Locate every blood parasite and identify its species.
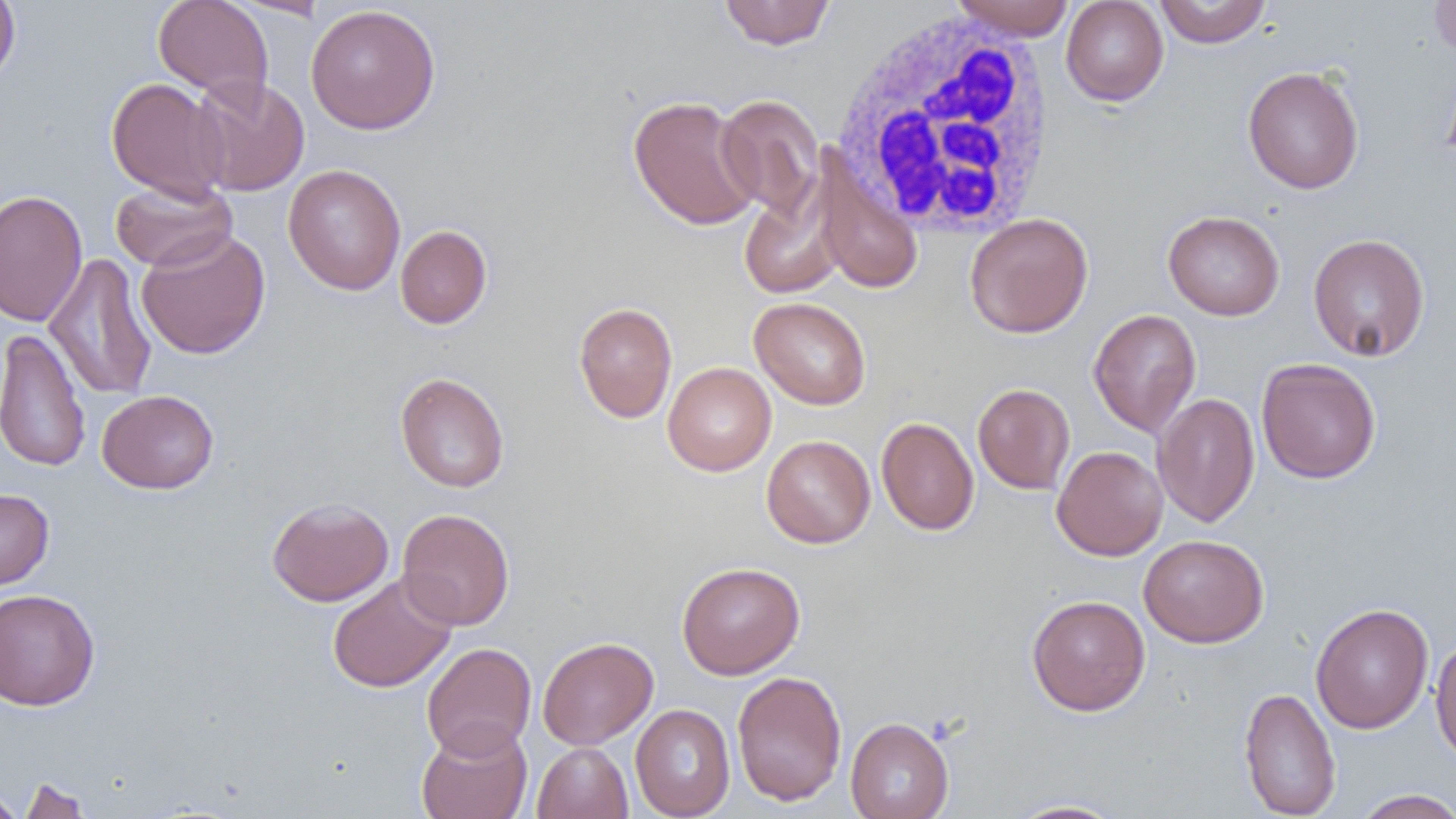
No blood parasites observed.

Summary:
  - Coordinate format: approximate bounding boxes as [x1, y1, x2, y2] in pixels
  - White blood cell locations: [828, 11, 1061, 242]
  - Uninfected red blood cell locations: [0, 0, 20, 87], [718, 0, 836, 50], [951, 0, 1076, 40], [1153, 0, 1272, 47], [1429, 0, 1456, 58], [153, 1, 273, 99], [1061, 1, 1169, 106], [305, 4, 441, 135], [1442, 62, 1456, 176], [1242, 66, 1364, 194], [189, 75, 310, 197], [106, 77, 230, 201], [716, 94, 825, 222], [628, 95, 761, 231], [812, 152, 924, 295], [283, 164, 406, 295], [109, 178, 237, 272], [739, 181, 847, 299], [0, 190, 87, 327], [1163, 210, 1285, 320], [964, 213, 1094, 338], [394, 225, 493, 328], [136, 228, 271, 360], [1307, 233, 1430, 362], [43, 253, 158, 400], [749, 297, 871, 409], [573, 302, 677, 423], [1088, 308, 1202, 437], [0, 328, 91, 473], [1256, 357, 1381, 484], [662, 362, 776, 476], [395, 372, 509, 493], [973, 383, 1075, 494], [97, 389, 219, 494], [1153, 392, 1260, 528], [877, 417, 979, 535], [761, 434, 876, 548], [1051, 445, 1168, 561], [0, 488, 54, 589], [267, 497, 394, 607], [397, 508, 515, 630], [1139, 534, 1269, 648], [676, 561, 805, 679], [327, 573, 457, 693], [0, 588, 100, 711], [1026, 594, 1151, 716], [1310, 603, 1434, 733], [537, 636, 658, 750], [1430, 636, 1456, 767], [421, 642, 536, 760], [731, 670, 848, 807], [1239, 686, 1341, 819], [630, 703, 736, 818], [845, 716, 954, 819], [416, 721, 533, 819], [531, 742, 633, 819], [16, 775, 92, 819], [0, 787, 25, 819], [1351, 788, 1456, 818], [1003, 799, 1128, 818]
  - Slide-level diagnosis: no evidence of blood parasites
  - Modality: optical microscopy
  - Image size: 1456×819 pixels
  - Field of view: one of a larger specimen
  - Magnification: 1000x
  - Preparation: thin blood film